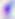

modality: photomicrograph
identification: Toxoplasma gondii
magnification: 400x